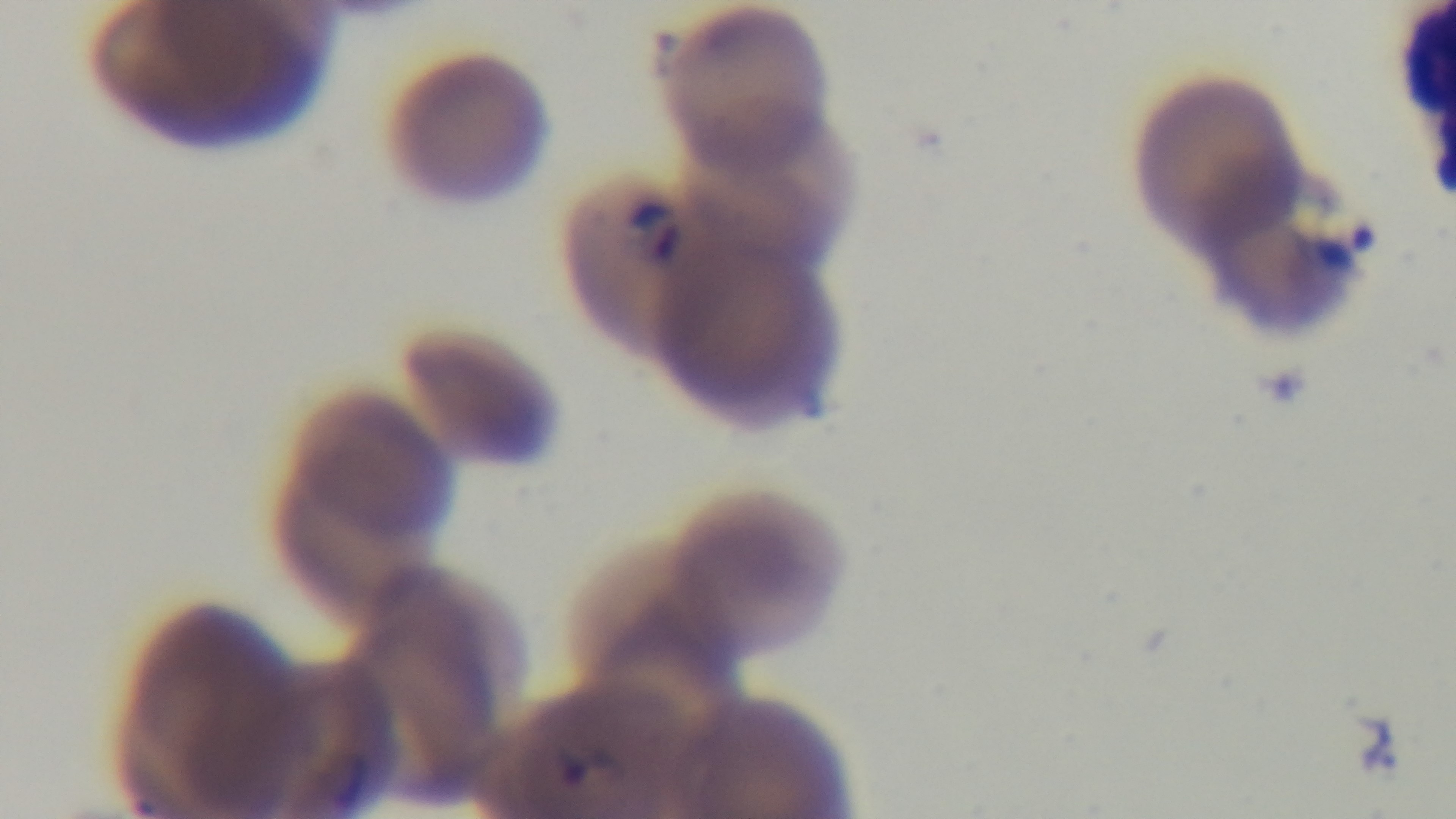
stain = Giemsa
field of view = one from the slide
modality = light microscopy
preparation = thin smear
capture = mounted 4K digital camera
objective = 100x oil immersion
malaria status = positive